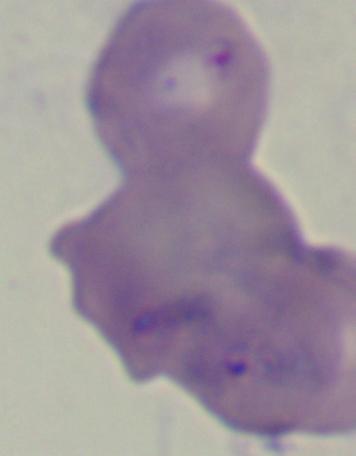
A Babesia parasite is seen. 1000x magnification. Photomicrograph.